Classify this cell by malaria status.
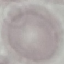
It is uninfected.

Thin blood smear. Giemsa-stained preparation. Cell patch, automatically extracted from a larger field of view and resized to 64 × 64 pixels. Acquired by smartphone through the microscope eyepiece.